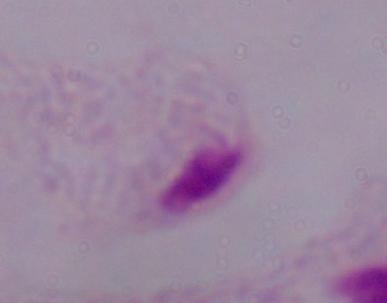
{
  "modality": "photomicrograph",
  "identification": "trichomonad",
  "magnification": "1000x"
}